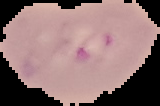 Segmented cell region on a black background. Result: malaria parasites identified. From a thin blood smear. Image is 160×106 pixels.